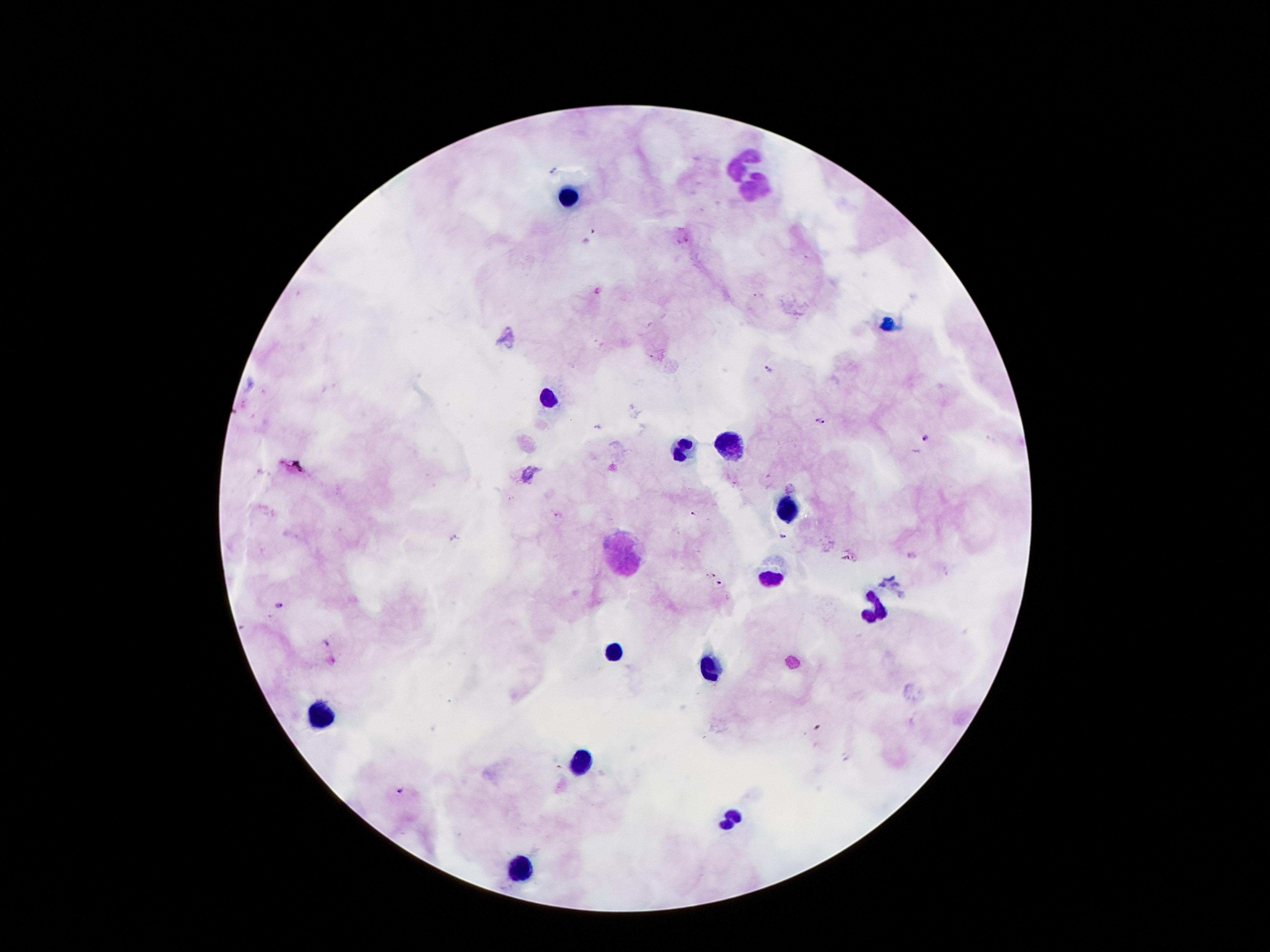
coordinate format = approximate centers as (x, y) in pixels
leukocyte locations = (745, 162), (756, 189), (568, 196), (552, 398), (738, 447), (677, 451), (783, 513), (624, 557), (770, 580), (876, 611), (615, 654), (709, 668), (322, 716), (584, 761), (731, 820), (524, 873)
malaria parasite locations = (769, 368), (821, 422), (927, 437), (694, 515), (785, 536), (712, 575), (720, 583), (325, 643), (401, 790)
capture = smartphone through the microscope eyepiece
stain = Giemsa
field of view = single
image size = 1270×952 pixels
magnification = 100x
preparation = thick blood film
patient malaria status = positive for Plasmodium falciparum